Describe the morphology of the erythrocytes.
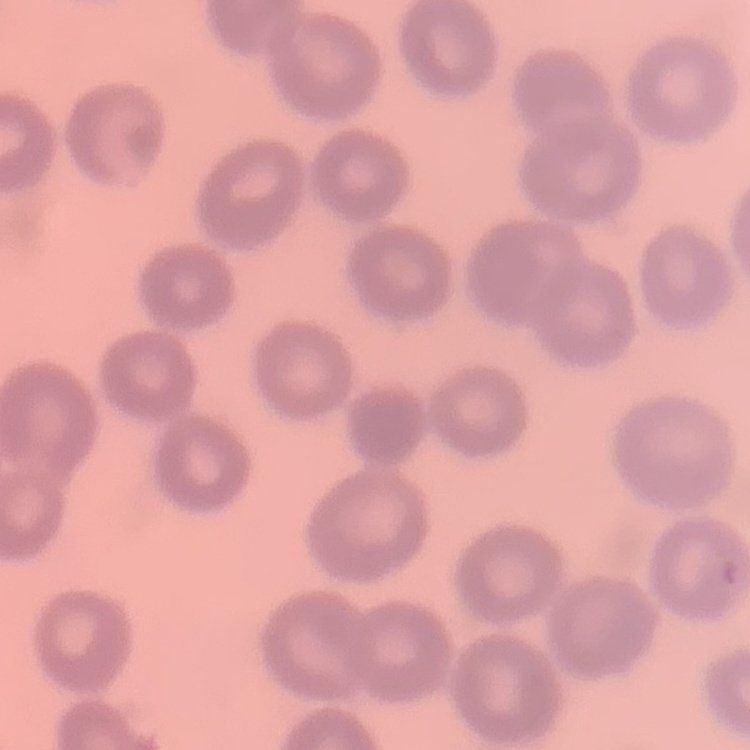

They show no rouleaux formation.

stain: Field's or Giemsa
image_type: square crop of a larger photomicrograph
preparation: thin blood smear